Locate every leukocyte (white blood cell).
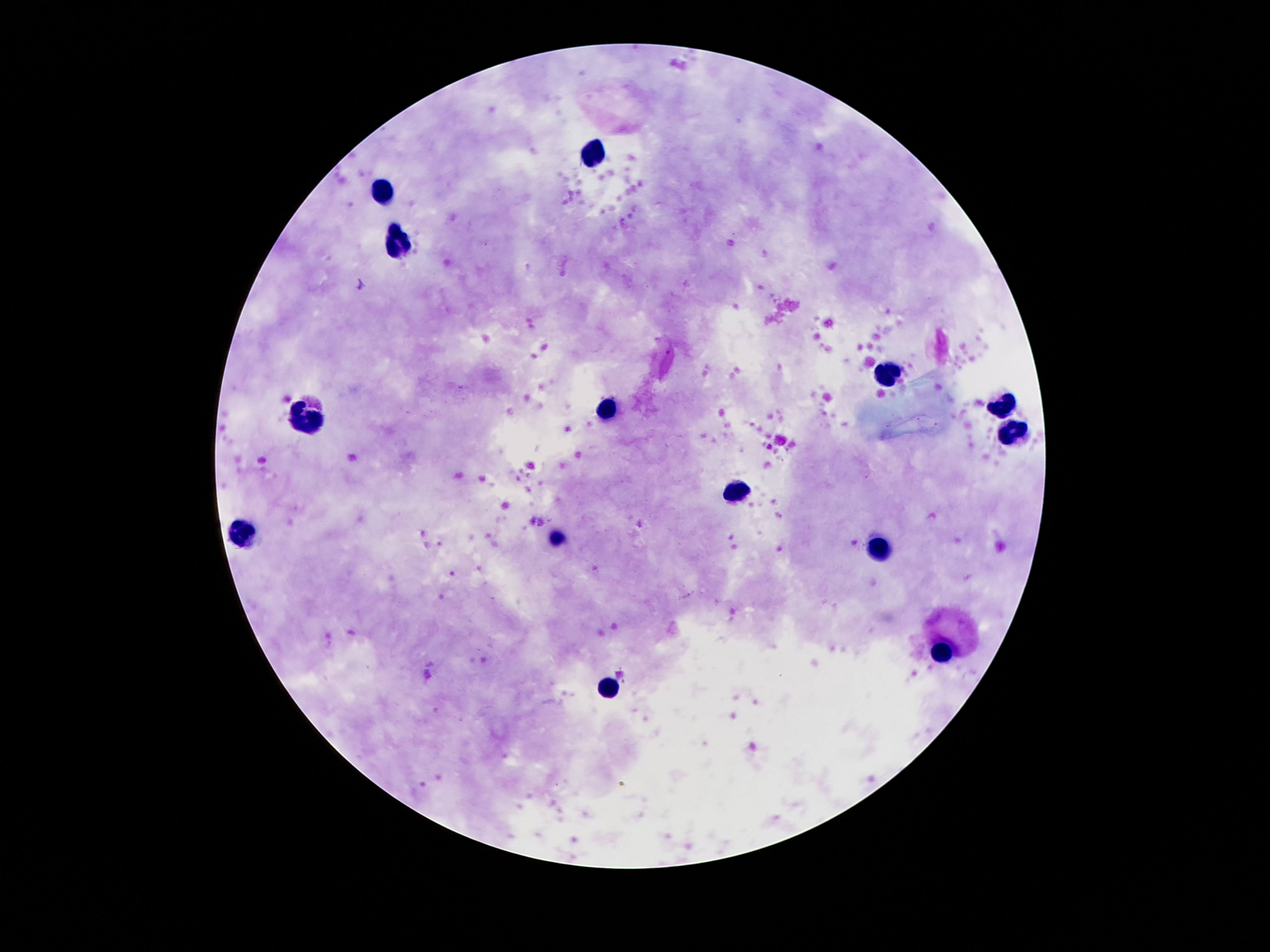
Approximate centers as [x, y] in pixels.
Leukocytes: [596, 155], [379, 190], [402, 245], [888, 373], [1005, 404], [603, 407], [304, 413], [1012, 435], [738, 490], [240, 532], [556, 537], [879, 547], [939, 652], [607, 689].

stain = Giemsa
patient malaria status = negative
preparation = thick peripheral-blood smear
field of view = single
capture = smartphone camera through the microscope eyepiece
image size = 1270×952 pixels
magnification = 100x